Identify the blood parasite species.
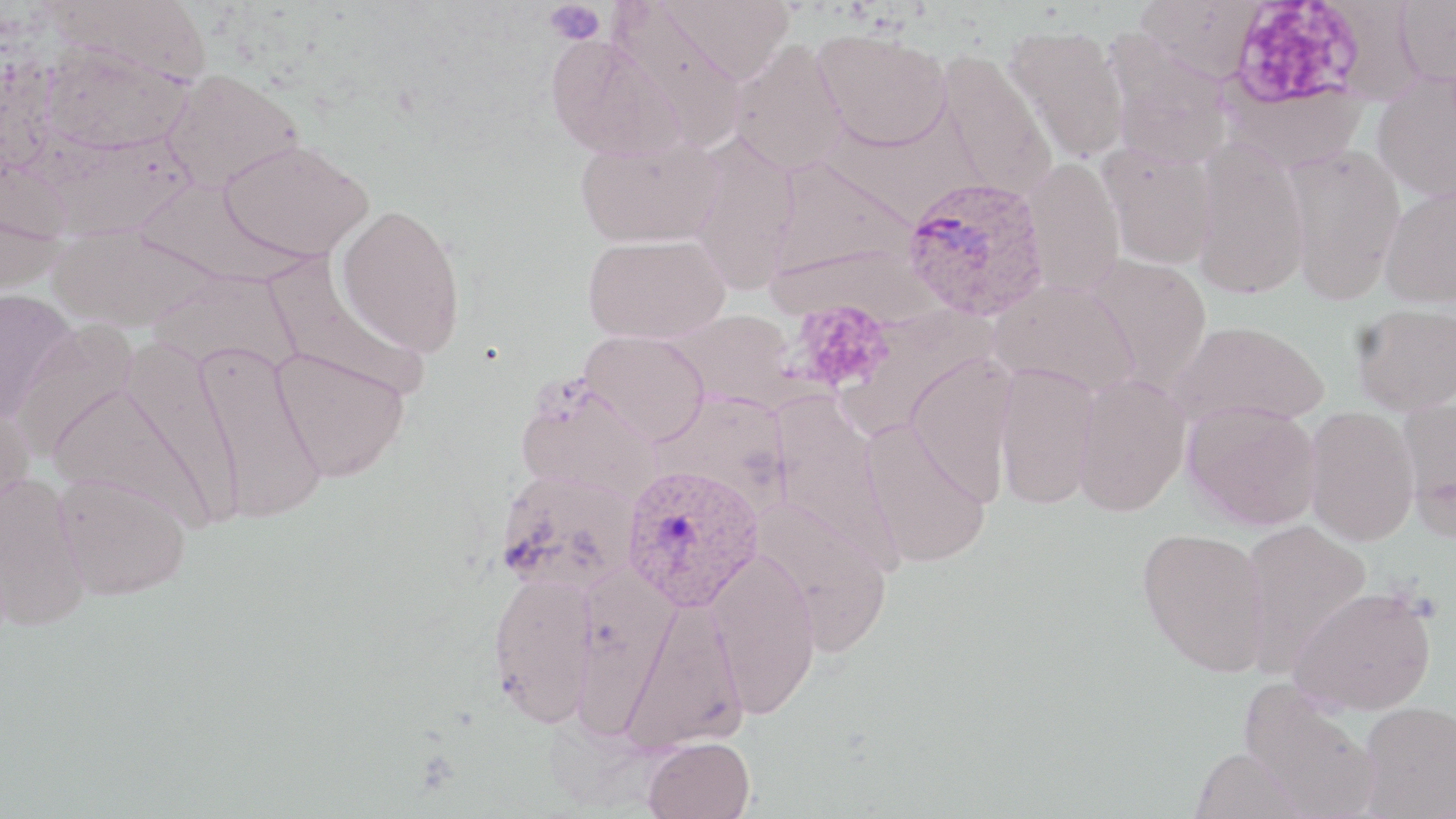

Plasmodium ovale.

Summary:
  - Coordinate format: approximate bounding boxes as (x1, y1, x2, y2) in pixels
  - Uninfected red blood cell locations: (660, 0, 794, 85), (1134, 0, 1263, 84), (1394, 1, 1456, 87), (610, 3, 747, 152), (1003, 24, 1129, 164), (813, 27, 951, 151), (1102, 30, 1233, 168), (546, 34, 683, 160), (39, 40, 193, 153), (729, 40, 848, 175), (935, 50, 1056, 199), (162, 68, 303, 193), (1372, 71, 1456, 203), (1219, 78, 1369, 171), (37, 130, 197, 242), (687, 133, 800, 295), (576, 137, 722, 248), (1192, 137, 1308, 300), (219, 139, 373, 262), (1282, 144, 1406, 302), (1101, 147, 1219, 269), (768, 157, 916, 284), (1021, 158, 1125, 297), (133, 178, 312, 288), (1379, 186, 1456, 309), (335, 203, 466, 357), (48, 225, 219, 332), (583, 233, 730, 343), (264, 255, 428, 400), (1082, 255, 1212, 395), (145, 270, 302, 375), (990, 282, 1139, 397), (0, 289, 76, 423), (1352, 302, 1456, 415), (4, 314, 131, 460), (1171, 319, 1329, 430), (581, 330, 709, 445), (118, 340, 245, 526), (192, 342, 327, 524), (271, 347, 411, 483), (906, 353, 1018, 505), (995, 364, 1099, 510), (1074, 373, 1190, 517), (45, 378, 225, 531), (516, 378, 659, 501), (772, 397, 906, 575), (1397, 397, 1456, 541), (1183, 400, 1321, 530), (0, 402, 34, 531), (1304, 406, 1419, 546), (858, 418, 994, 570), (495, 469, 639, 595), (53, 472, 191, 601), (0, 474, 91, 632), (751, 501, 895, 655), (1240, 519, 1372, 673), (1137, 527, 1271, 677), (705, 551, 821, 718), (488, 570, 599, 726), (572, 570, 679, 738), (1289, 586, 1437, 715), (619, 595, 750, 755), (1238, 680, 1381, 819), (1358, 701, 1456, 819), (643, 736, 755, 819), (1191, 747, 1309, 819)
  - Plasmodium ovale-infected red blood cell locations: (902, 176, 1050, 320), (622, 463, 764, 612)
  - Platelet locations: (543, 0, 606, 45), (793, 300, 895, 395)
  - Image size: 1456×819 pixels
  - Field of view: single
  - Preparation: thin blood film
  - Magnification: 1000x
  - Stain: May-Grünwald-Giemsa
  - Modality: light microscopy